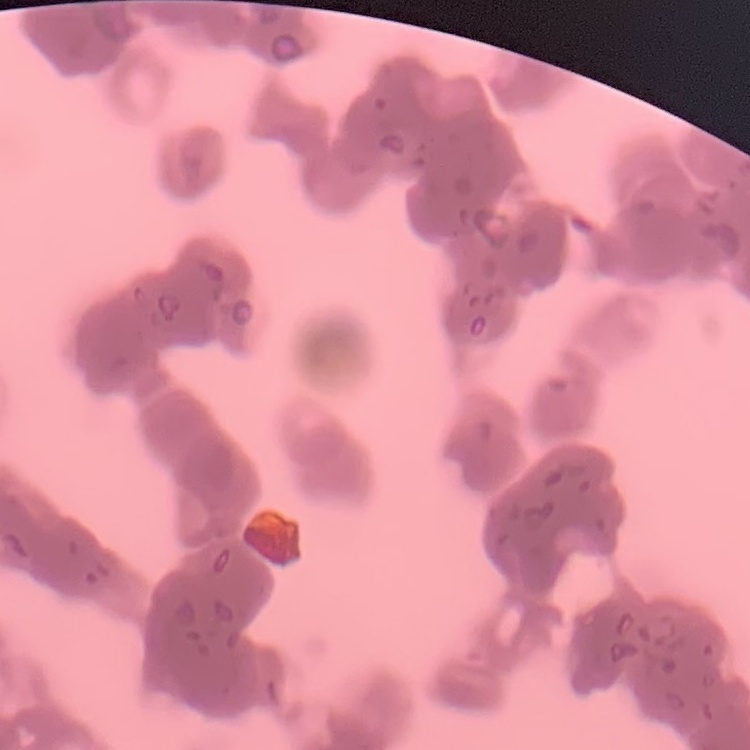
Summary:
  - Erythrocyte morphology: rouleaux formation
  - Preparation: thin blood smear
  - Image type: square crop of a larger photomicrograph
  - Stain: Field's or Giemsa